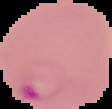

{
  "image_size": "112×109 pixels",
  "result": "Plasmodium parasites detected",
  "image_type": "cell region segmented out of the field of view; surrounding area masked to black",
  "preparation": "thin blood film"
}